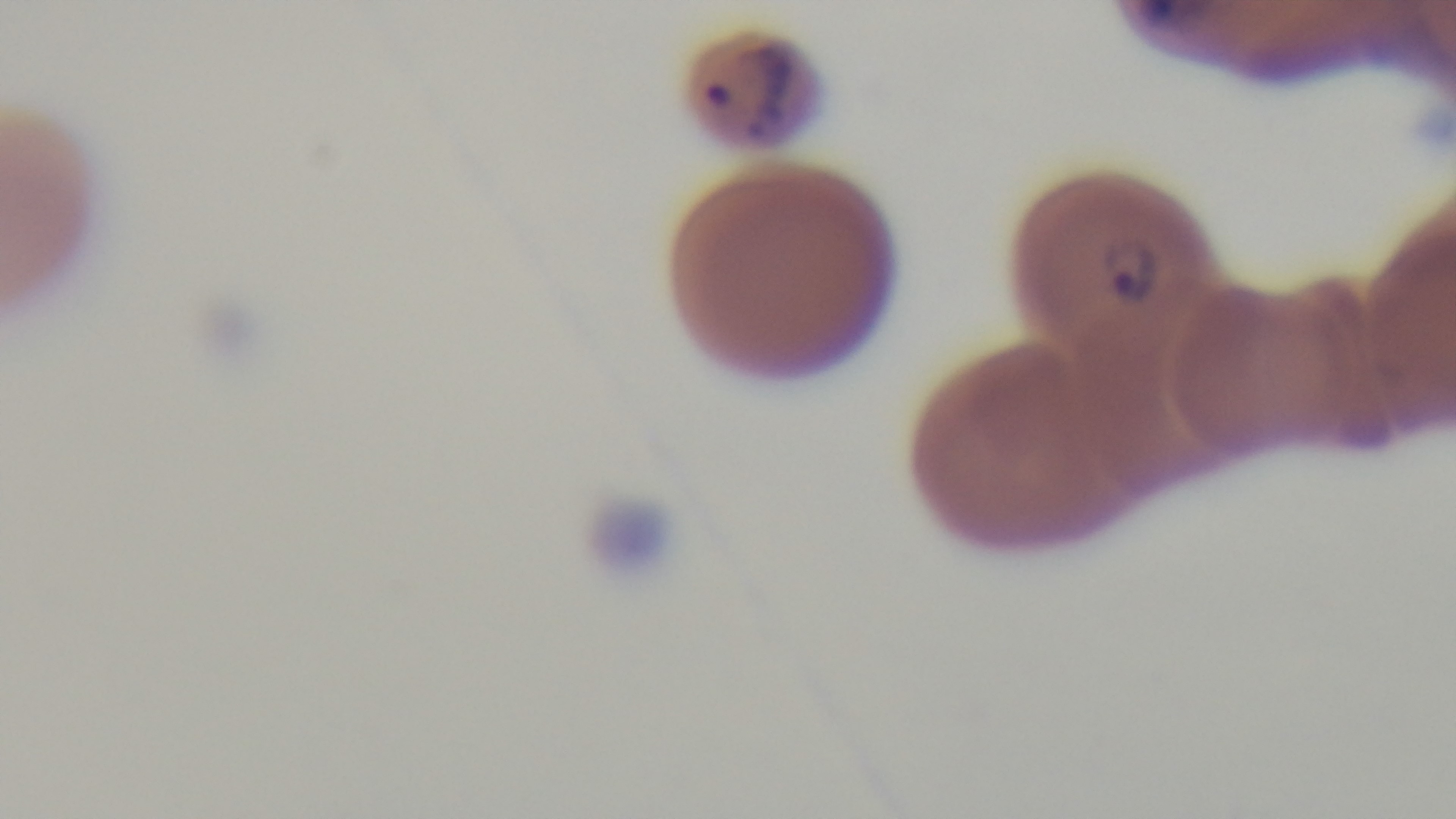

Summary:
  - Preparation: thin
  - Objective: 100x oil immersion
  - Malaria status: infected
  - Capture: mounted 4K digital camera
  - Field of view: one from the slide
  - Stain: Giemsa
  - Modality: light microscopy